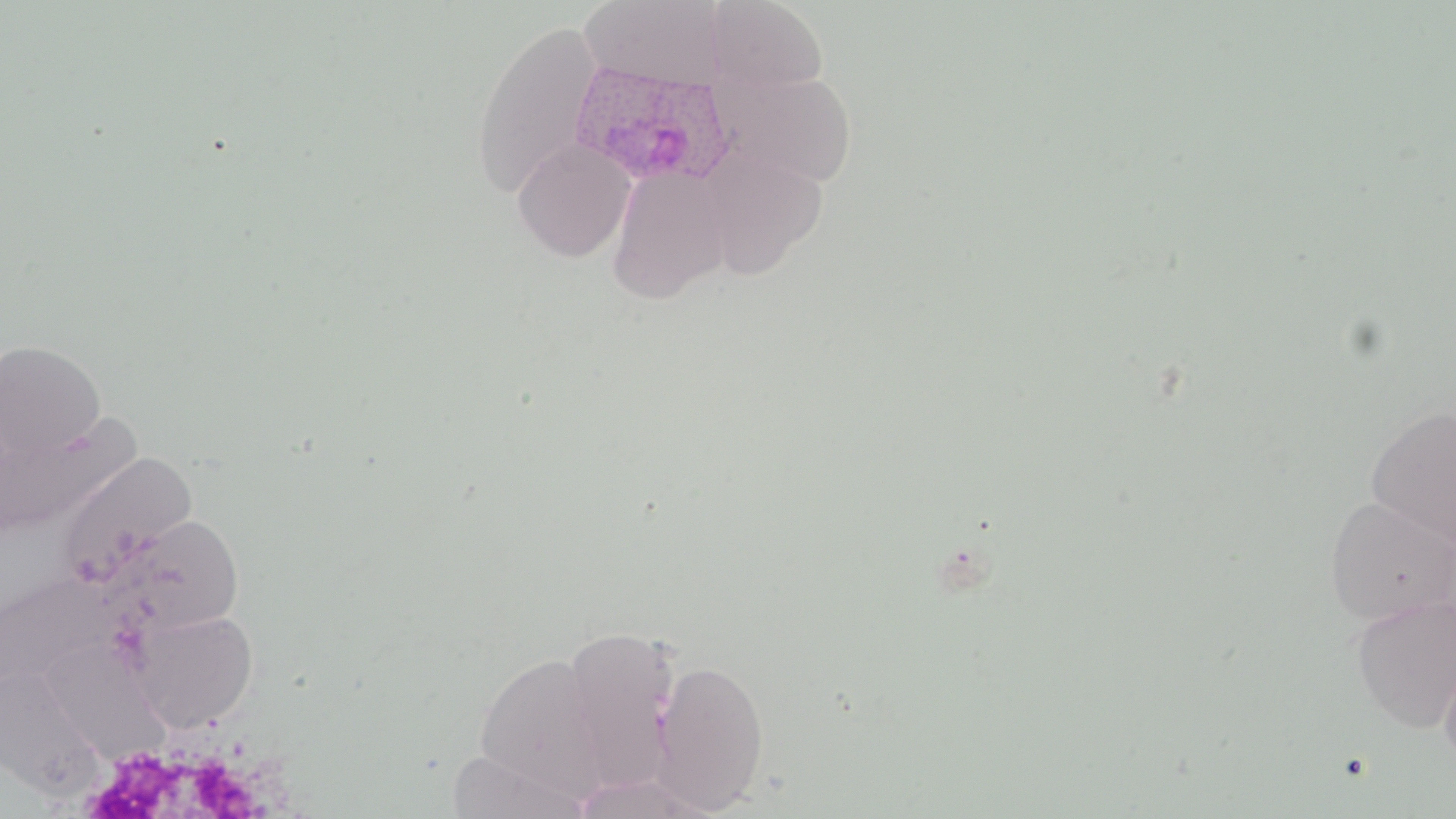

Summary:
  - Coordinate format: approximate bounding boxes as (x1,y1)-(x2,y2) corner pairs in pixels
  - Uninfected red blood cell locations: (577,0)-(729,91), (706,0)-(830,94), (469,20)-(605,201), (723,69)-(859,188), (513,139)-(637,262), (607,164)-(733,302), (0,339)-(106,462), (1366,405)-(1456,549), (0,411)-(133,538), (55,451)-(197,591), (1322,494)-(1456,626), (106,512)-(246,637), (0,570)-(121,697), (1350,594)-(1456,732), (128,608)-(259,732), (560,625)-(682,794), (36,638)-(175,770), (1438,642)-(1456,774), (472,650)-(612,796), (652,657)-(770,814), (0,663)-(105,799), (446,749)-(593,819), (568,771)-(720,818)
  - Plasmodium ovale-infected red blood cell locations: (568,61)-(736,188)
  - Slide-level diagnosis: Plasmodium ovale
  - Image size: 1456×819 pixels
  - Preparation: thin blood film
  - Modality: light microscopy
  - Field of view: single
  - Stain: May-Grünwald-Giemsa
  - Magnification: 1000x